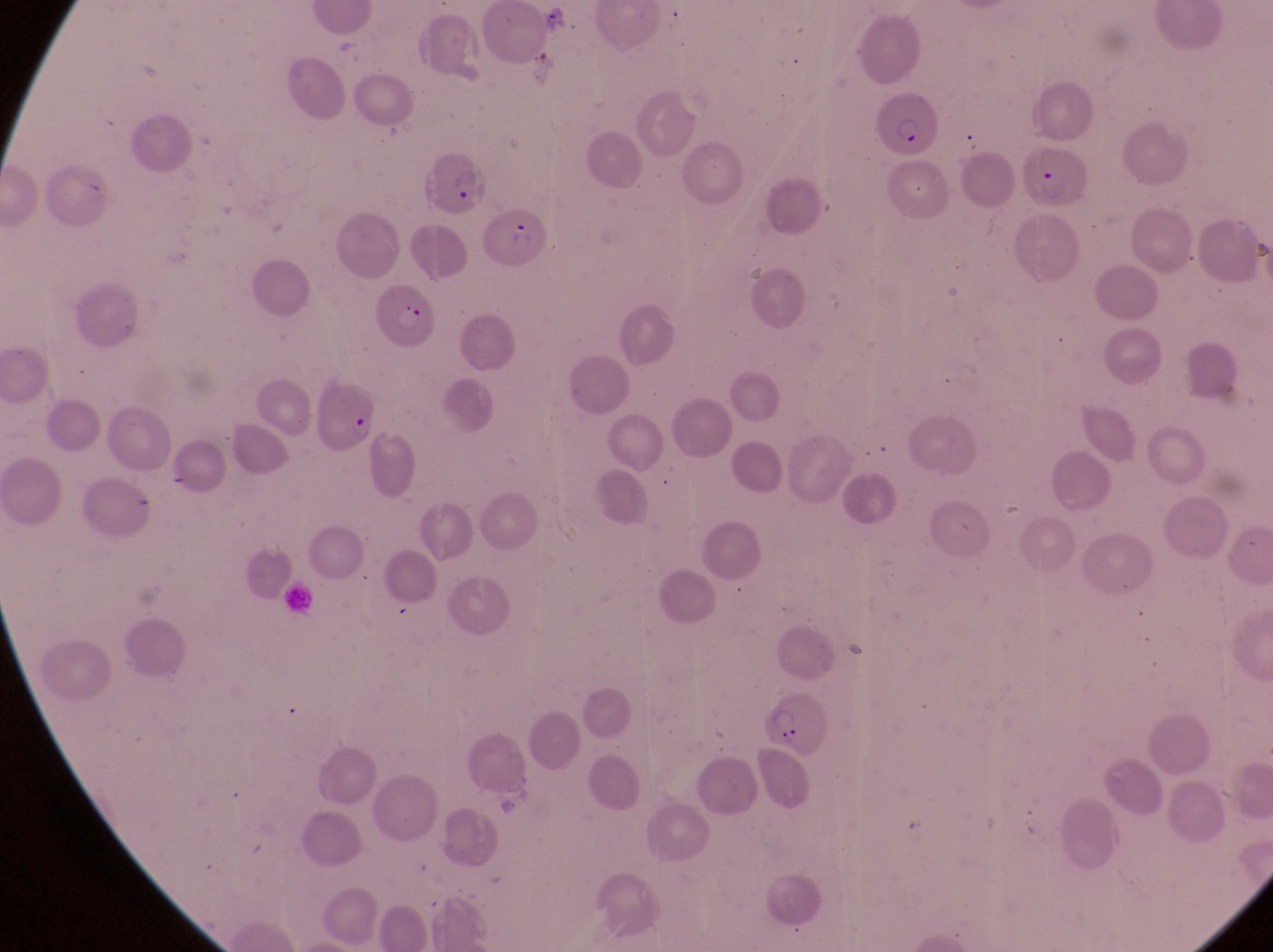
capture: smartphone photograph through the eyepiece of an Olympus CX-23 microscope
preparation: thin blood film
trophozoite_locations: 'approximate bounding boxes as {left, top, right, bottom} in pixels: {541, 3, 569, 36}'
field_of_view: single
country: Uganda
parasitised_red_blood_cell_locations: 'approximate bounding boxes as {left, top, right, bottom} in pixels: {876, 93, 936, 156}, {1031, 140, 1094, 214}, {419, 150, 488, 215}, {487, 204, 554, 272}, {375, 280, 437, 358}, {307, 372, 381, 454}, {762, 694, 831, 759}'
image_size: 1273×952 pixels
magnification: 1000x